State which parasite is depicted.
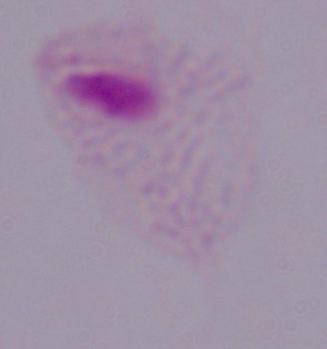
This is a trichomonad.

Photomicrograph. Captured at 1000x magnification.